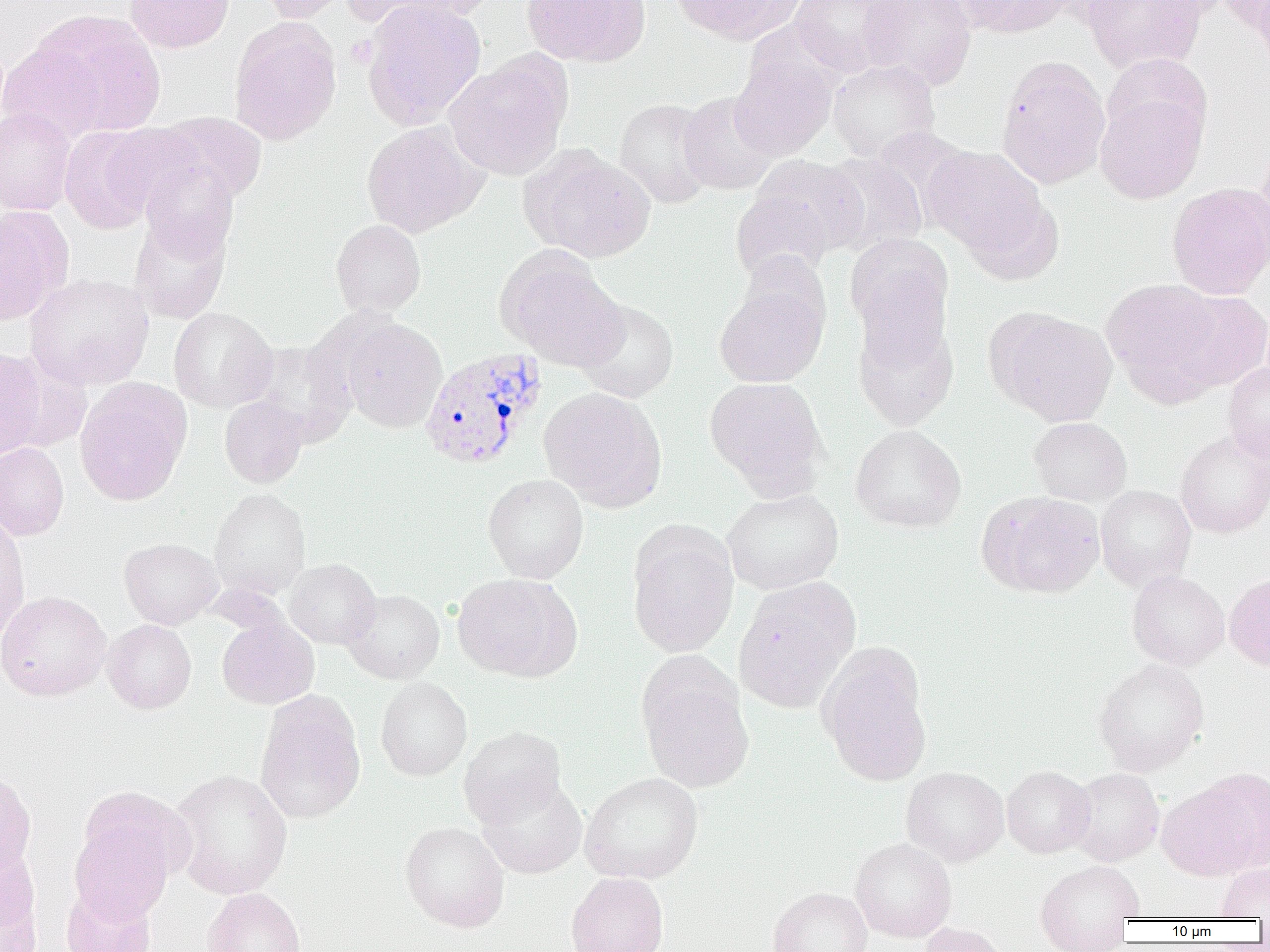

slide-level diagnosis = Plasmodium vivax
uninfected red blood cell locations = approximate bounding boxes as (x1, y1, x2, y2) in pixels: (124, 0, 234, 53), (254, 0, 353, 23), (345, 0, 485, 34), (521, 0, 650, 67), (669, 0, 804, 44), (789, 0, 909, 77), (859, 0, 978, 90), (954, 0, 1077, 38), (1081, 0, 1206, 73), (1218, 0, 1270, 39), (1251, 0, 1270, 69), (361, 1, 486, 129), (29, 10, 165, 137), (229, 17, 342, 145), (0, 42, 107, 144), (730, 53, 837, 160), (1102, 53, 1212, 149), (445, 55, 571, 179), (995, 56, 1111, 189), (828, 59, 939, 161), (678, 91, 780, 196), (1095, 91, 1207, 204), (614, 98, 717, 209), (0, 107, 75, 216), (148, 112, 267, 207), (362, 122, 485, 238), (59, 125, 162, 233), (1255, 142, 1270, 255), (922, 145, 1047, 257), (524, 148, 655, 263), (818, 152, 927, 257), (747, 155, 869, 259), (137, 157, 240, 260), (1166, 182, 1270, 300), (730, 188, 835, 283), (0, 206, 72, 324), (129, 214, 232, 323), (331, 219, 426, 317), (845, 234, 954, 349), (497, 250, 626, 370), (25, 273, 154, 390), (1101, 277, 1227, 401), (715, 278, 828, 387), (1166, 290, 1270, 392), (575, 299, 679, 402), (852, 306, 959, 432), (168, 307, 277, 412), (991, 309, 1118, 426), (340, 319, 447, 433), (246, 341, 356, 445), (0, 349, 48, 458), (1223, 362, 1270, 465), (704, 376, 828, 496), (74, 378, 192, 507), (539, 387, 667, 509), (219, 395, 308, 488), (1028, 417, 1133, 506), (850, 424, 967, 533), (1175, 429, 1270, 539), (0, 442, 69, 541), (483, 473, 589, 583), (1095, 485, 1196, 590), (722, 487, 844, 594), (209, 488, 311, 600), (979, 492, 1104, 598), (0, 512, 30, 643), (627, 523, 739, 657), (119, 538, 223, 629), (283, 558, 381, 649), (1127, 570, 1229, 669), (452, 573, 581, 681), (1224, 573, 1270, 671), (732, 577, 860, 713), (342, 589, 445, 684), (0, 591, 111, 701), (217, 616, 319, 709), (102, 620, 196, 714), (817, 646, 932, 786), (637, 656, 755, 794), (1093, 658, 1209, 775), (375, 677, 472, 781), (255, 693, 366, 824), (458, 725, 567, 827), (1001, 765, 1095, 858), (901, 766, 1009, 866), (1068, 768, 1164, 866), (0, 769, 36, 879), (169, 769, 293, 899), (1157, 770, 1270, 881), (580, 772, 703, 884), (477, 775, 587, 878), (76, 785, 193, 886), (70, 818, 177, 921), (400, 821, 510, 932), (850, 837, 956, 943), (0, 841, 44, 951), (1034, 859, 1144, 950), (1216, 862, 1270, 920), (566, 872, 669, 952), (60, 885, 157, 952), (768, 886, 873, 952), (201, 887, 306, 952), (918, 922, 1008, 952)
image size = 1270×952 pixels
field of view = single
preparation = thin blood smear
Plasmodium vivax-infected red blood cell locations = approximate bounding boxes as (x1, y1, x2, y2) in pixels: (419, 346, 548, 470)
platelet locations = approximate bounding boxes as (x1, y1, x2, y2) in pixels: (345, 36, 377, 68)
modality = optical microscopy
magnification = 1000x